Assess this cell for malaria.
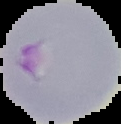

It is parasitized.

preparation = thin blood film
image type = segmented cell region with the area outside set to black
image size = 121×124 pixels